Name the blood parasite species.
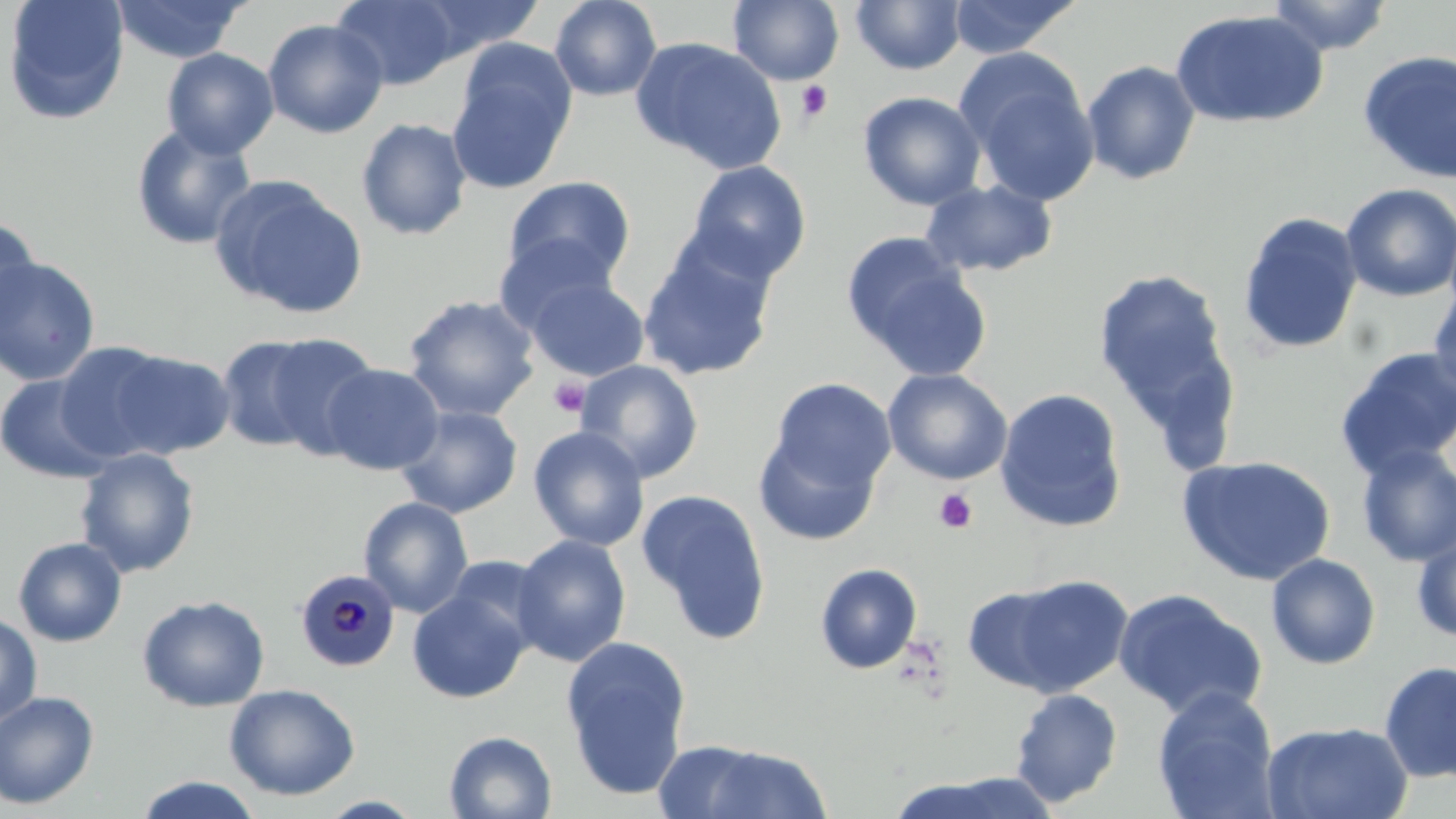
Plasmodium malariae.

Approximate bounding boxes as (x1, y1, x2, y2) in pixels. Plasmodium malariae-infected red blood cell locations: (295, 568, 399, 671). Platelet locations: (797, 80, 833, 121), (548, 377, 591, 419), (934, 489, 978, 534). Uninfected red blood cell locations: (2, 0, 129, 125), (111, 0, 248, 64), (414, 0, 545, 59), (548, 0, 663, 102), (947, 0, 1083, 59), (1266, 0, 1392, 56), (331, 1, 464, 89), (728, 1, 844, 86), (850, 1, 967, 75), (1170, 9, 1328, 129), (263, 18, 389, 139), (631, 36, 787, 173), (161, 48, 279, 159), (1358, 50, 1456, 185), (447, 54, 575, 196), (959, 55, 1101, 207), (1082, 60, 1201, 185), (857, 91, 986, 210), (355, 117, 473, 241), (130, 123, 259, 250), (685, 160, 812, 282), (210, 175, 368, 320), (503, 176, 637, 285), (919, 179, 1058, 278), (1340, 183, 1456, 301), (1237, 211, 1363, 356), (0, 214, 40, 336), (493, 234, 619, 335), (637, 240, 778, 382), (852, 252, 991, 382), (0, 255, 101, 386), (1093, 269, 1232, 414), (525, 276, 649, 381), (1427, 286, 1456, 400), (402, 294, 540, 422), (256, 332, 382, 459), (216, 334, 329, 454), (54, 342, 177, 464), (1335, 346, 1456, 478), (108, 348, 236, 458), (573, 360, 704, 484), (322, 363, 444, 475), (882, 368, 1012, 486), (0, 373, 114, 484), (767, 377, 895, 492), (994, 387, 1128, 532), (394, 404, 523, 518), (528, 426, 650, 552), (753, 428, 882, 546), (1355, 444, 1456, 568), (74, 447, 201, 578), (1176, 454, 1336, 585), (636, 488, 772, 644), (358, 496, 474, 618), (1412, 529, 1456, 643), (511, 533, 631, 667), (13, 536, 128, 647), (441, 553, 554, 651), (1266, 553, 1381, 670), (814, 563, 923, 675), (973, 574, 1135, 699), (407, 586, 532, 703), (1112, 588, 1268, 720), (136, 594, 270, 712), (0, 611, 42, 728), (560, 637, 692, 799), (1378, 660, 1456, 784), (224, 683, 361, 800), (1152, 687, 1279, 818), (1009, 688, 1123, 807), (0, 690, 100, 811), (1262, 721, 1414, 819), (443, 730, 557, 818), (684, 742, 832, 819), (884, 771, 1062, 819), (132, 775, 266, 818). Optical microscopy. Single field of view. May-Grünwald-Giemsa-stained preparation. Thin blood smear. Captured at 1000x magnification. Image is 1456×819 pixels.